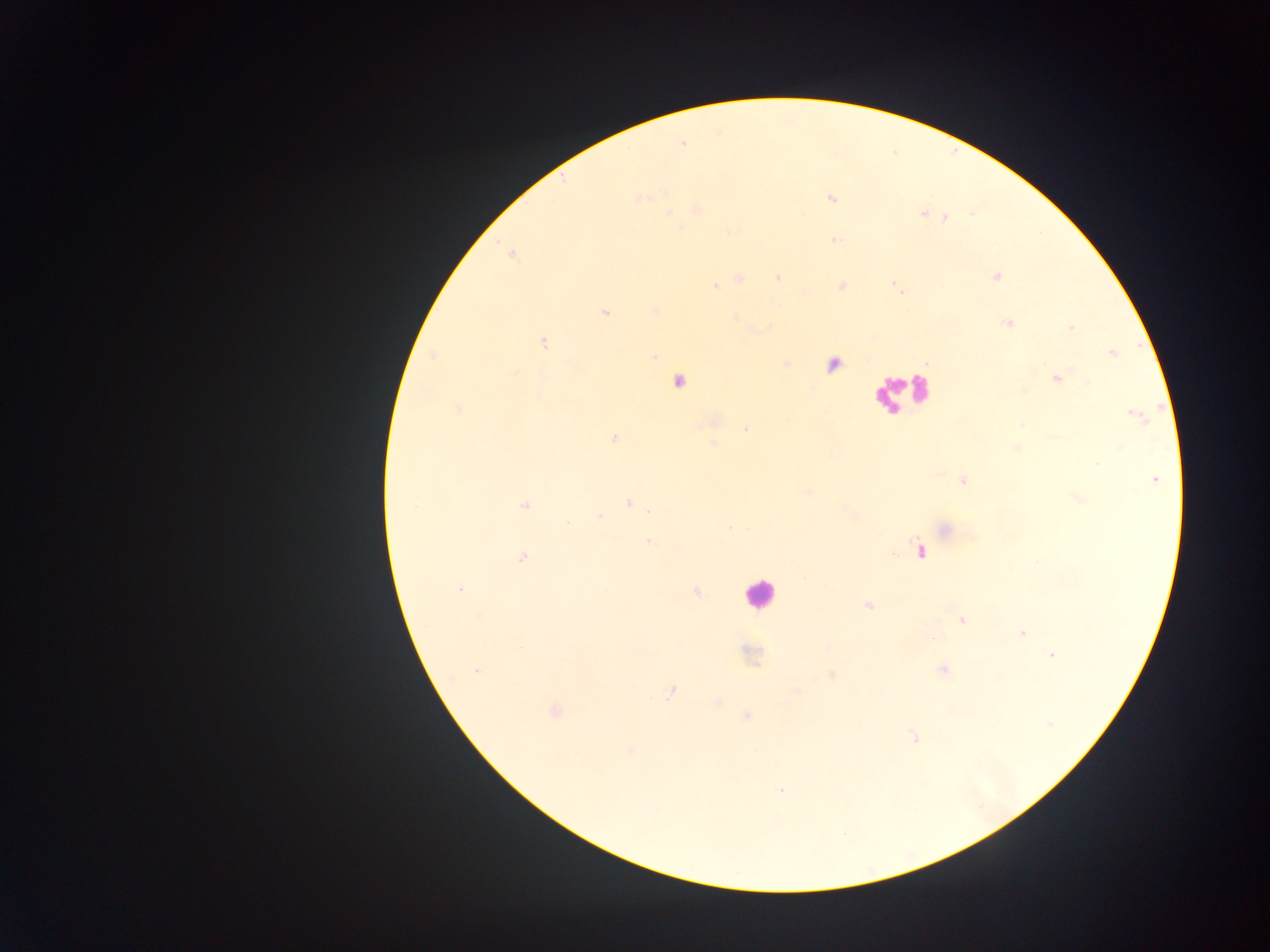

{
  "malaria_parasite_locations": "approximate centers as {x, y} in pixels: {683, 143}, {831, 198}, {638, 199}, {922, 213}, {671, 214}, {946, 218}, {833, 239}, {996, 276}, {739, 278}, {778, 278}, {715, 286}, {842, 286}, {896, 286}, {655, 309}, {604, 312}, {735, 317}, {1008, 323}, {1071, 328}, {544, 343}, {1113, 353}, {433, 356}, {653, 357}, {515, 374}, {1058, 378}, {679, 381}, {457, 409}, {1135, 415}, {1022, 425}, {745, 429}, {1054, 436}, {614, 438}, {712, 443}, {1017, 448}, {1155, 479}, {963, 481}, {807, 492}, {1078, 498}, {630, 503}, {524, 506}, {849, 513}, {600, 517}, {567, 523}, {729, 528}, {944, 530}, {650, 541}, {919, 551}, {523, 557}, {461, 589}, {696, 592}, {868, 606}, {478, 615}, {961, 620}, {1022, 633}, {828, 647}, {520, 648}, {1052, 655}, {942, 670}, {477, 671}, {832, 675}, {797, 691}, {670, 692}, {553, 711}, {746, 716}, {1050, 723}, {913, 737}, {630, 750}, {781, 791}",
  "field_of_view": "single",
  "capture": "mobile-phone photograph through a microscope",
  "country": "Ghana",
  "leukocyte_locations": "approximate centers as {x, y} in pixels: {897, 391}, {758, 594}",
  "image_size": "1270×952 pixels",
  "preparation": "thick blood smear"
}